State which cell type is depicted.
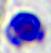
A leukocyte.

Captured at 400x magnification. Photomicrograph.